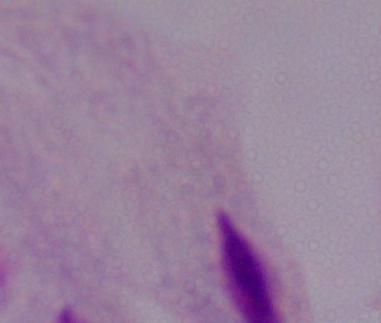

modality = micrograph
magnification = 1000x
identification = trichomonad